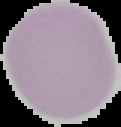

Summary:
  - Preparation: thin blood smear
  - Result: negative for Plasmodium parasites
  - Image type: segmented cell region with the area outside set to black
  - Image size: 121×127 pixels